Report the malaria status of this cell.
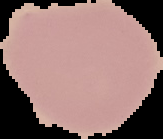
It is uninfected.

Summary:
  - Image type: segmented cell region with the area outside set to black
  - Preparation: thin blood film
  - Image size: 163×139 pixels